Point out each Plasmodium parasite.
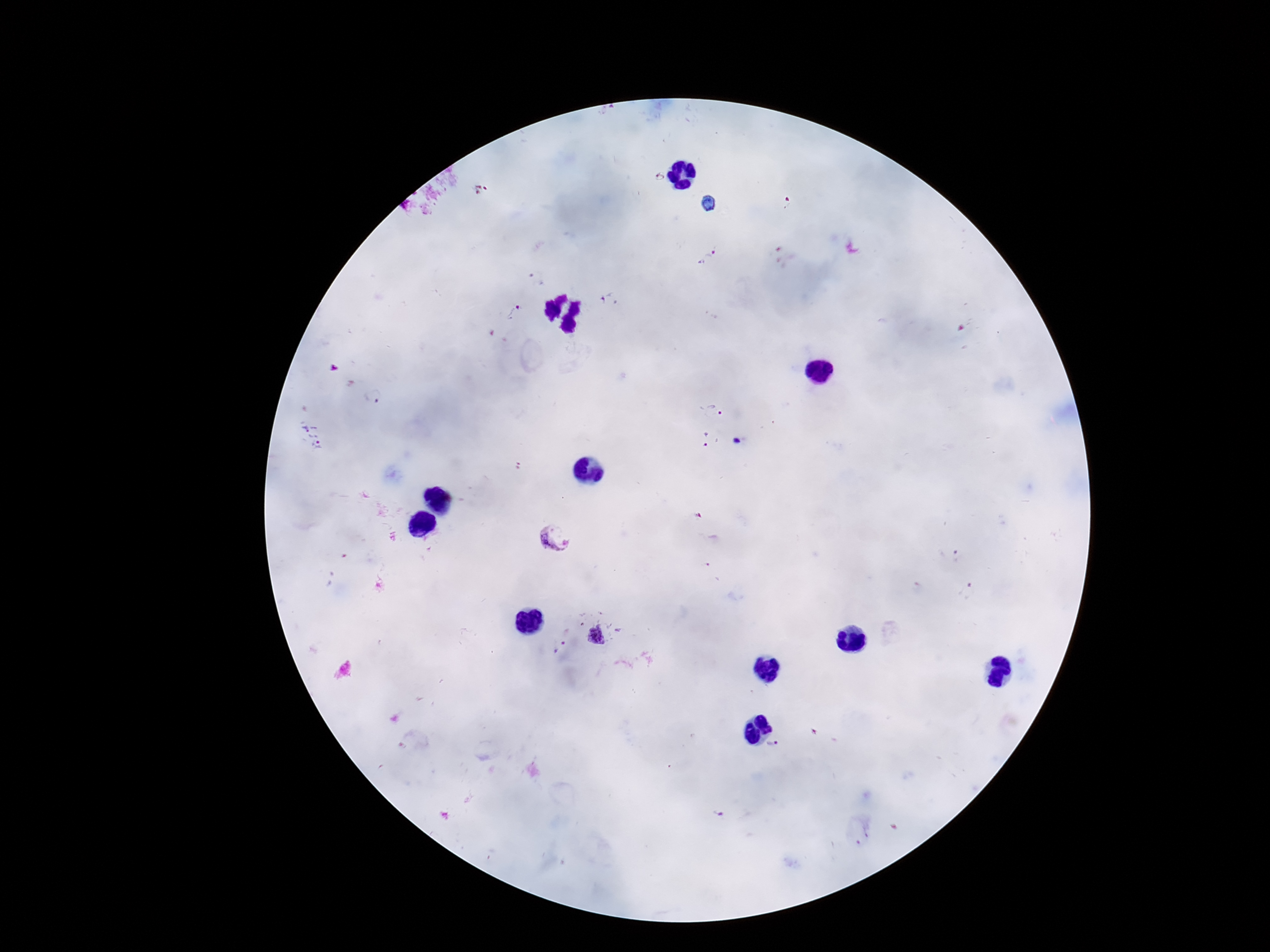

Approximate centers as {x, y} in pixels.
Plasmodium parasites: {715, 410}, {703, 439}, {560, 539}, {597, 636}, {559, 647}, {772, 743}.

Summary:
  - Magnification: 100x
  - Patient malaria status: positive
  - Preparation: thick blood film
  - Stain: Giemsa
  - Field of view: single
  - Image size: 1270×952 pixels
  - Capture: smartphone camera through the microscope eyepiece